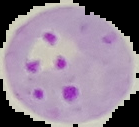 Image is 139×127 pixels. Result: malaria parasites detected. From a thin blood smear. The area outside the segmented cell region is set to black.